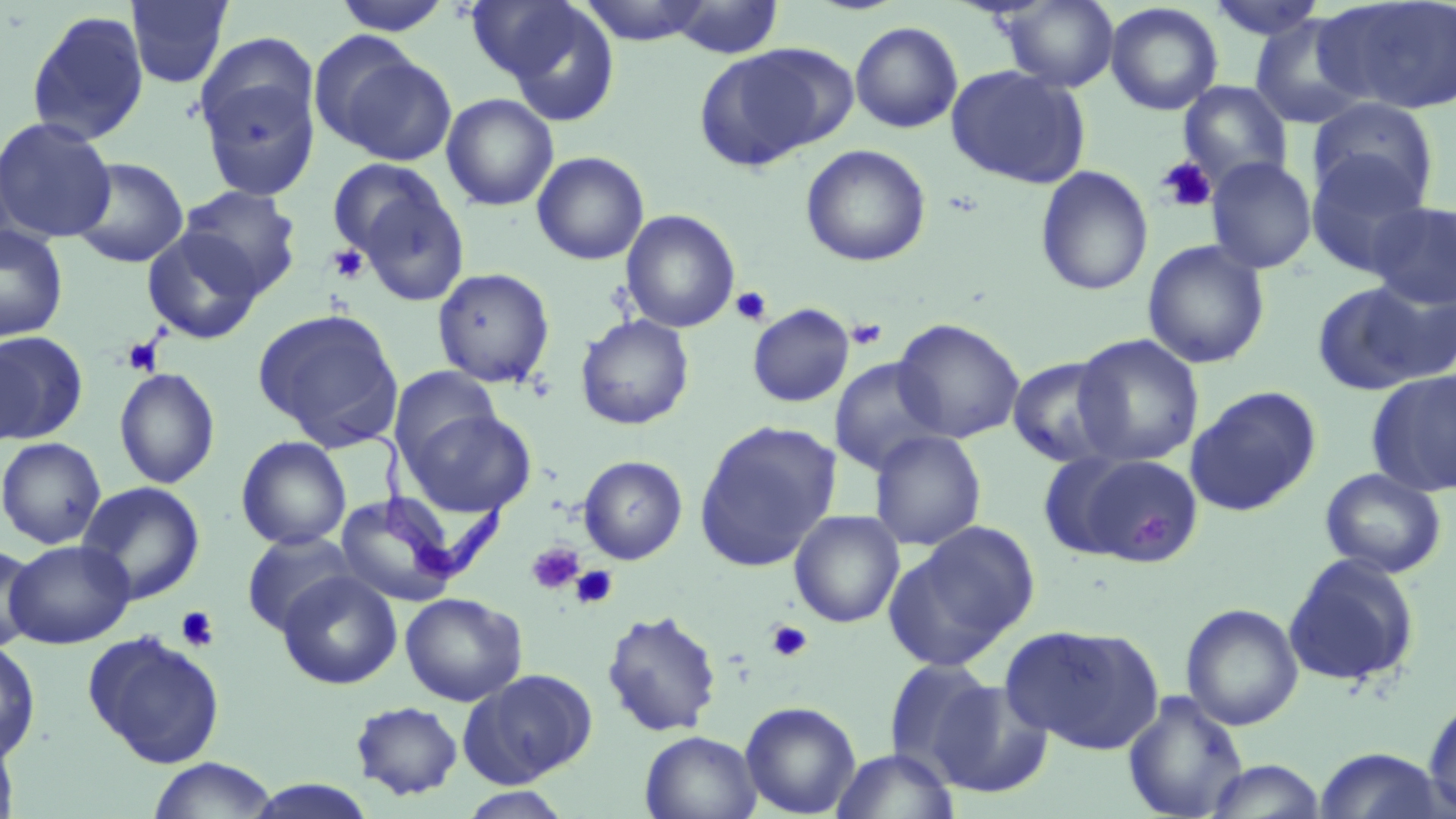

Trypanosoma brucei locations = approximate bounding boxes as (x1,y1)-(x2,y2) corner pairs in pixels: (334,414)-(510,590)
slide-level diagnosis = Trypanosoma brucei
preparation = thin blood smear
stain = May-Grünwald-Giemsa
field of view = single
platelet locations = approximate bounding boxes as (x1,y1)-(x2,y2) corner pairs in pixels: (1156,156)-(1218,213), (327,244)-(369,285), (731,286)-(772,326), (846,318)-(888,350), (121,336)-(164,376), (1128,513)-(1171,549), (526,542)-(584,595), (570,566)-(618,610), (176,606)-(219,651), (766,620)-(814,662)
uninfected red blood cell locations = approximate bounding boxes as (x1,y1)-(x2,y2) corner pairs in pixels: (124,0)-(234,89), (481,0)-(622,124), (576,0)-(715,45), (1206,0)-(1328,42), (1315,0)-(1456,116), (332,1)-(454,35), (666,1)-(784,59), (999,1)-(1119,92), (1104,2)-(1223,116), (25,9)-(150,147), (1247,14)-(1375,130), (850,21)-(963,134), (195,39)-(321,197), (320,43)-(457,166), (694,46)-(841,172), (946,64)-(1090,189), (1178,81)-(1292,188), (441,93)-(559,212), (1308,97)-(1439,210), (0,117)-(117,243), (801,144)-(931,267), (1306,150)-(1430,276), (531,151)-(649,266), (1205,156)-(1317,274), (70,157)-(189,269), (1035,165)-(1154,296), (340,171)-(470,306), (178,185)-(302,298), (1367,200)-(1456,308), (620,210)-(741,333), (0,224)-(69,342), (142,229)-(265,345), (1142,240)-(1270,369), (432,267)-(555,388), (1311,281)-(1441,395), (747,303)-(855,407), (253,308)-(404,450), (575,315)-(695,430), (892,318)-(1025,444), (0,332)-(88,444), (1072,334)-(1205,467), (0,343)-(31,449), (1006,356)-(1123,469), (828,357)-(948,475), (390,366)-(502,471), (114,367)-(220,489), (1366,369)-(1456,497), (1185,385)-(1321,518), (405,407)-(537,516), (694,420)-(841,571), (868,430)-(986,551), (236,435)-(352,551), (0,437)-(106,549), (1059,452)-(1205,567), (578,455)-(688,564), (1320,467)-(1447,579), (76,481)-(206,605), (335,492)-(463,607), (789,510)-(905,628), (887,522)-(1040,668), (241,531)-(358,636), (4,539)-(136,649), (0,542)-(43,652), (1283,553)-(1420,688), (277,570)-(403,690), (400,592)-(527,706), (1180,603)-(1304,731), (600,609)-(723,738), (1001,623)-(1163,754), (83,630)-(224,767), (0,639)-(41,765), (883,658)-(1000,782), (461,669)-(596,787), (929,679)-(1055,798), (1122,690)-(1250,818), (1422,697)-(1456,817), (350,700)-(464,800), (740,700)-(861,817), (639,730)-(762,818), (0,733)-(20,819), (1311,746)-(1453,818), (831,747)-(959,819), (147,757)-(278,818), (1201,759)-(1329,818), (241,779)-(380,818), (457,787)-(574,819)
modality = optical microscopy
magnification = 1000x
image size = 1456×819 pixels